Locate every uninfected red blood cell.
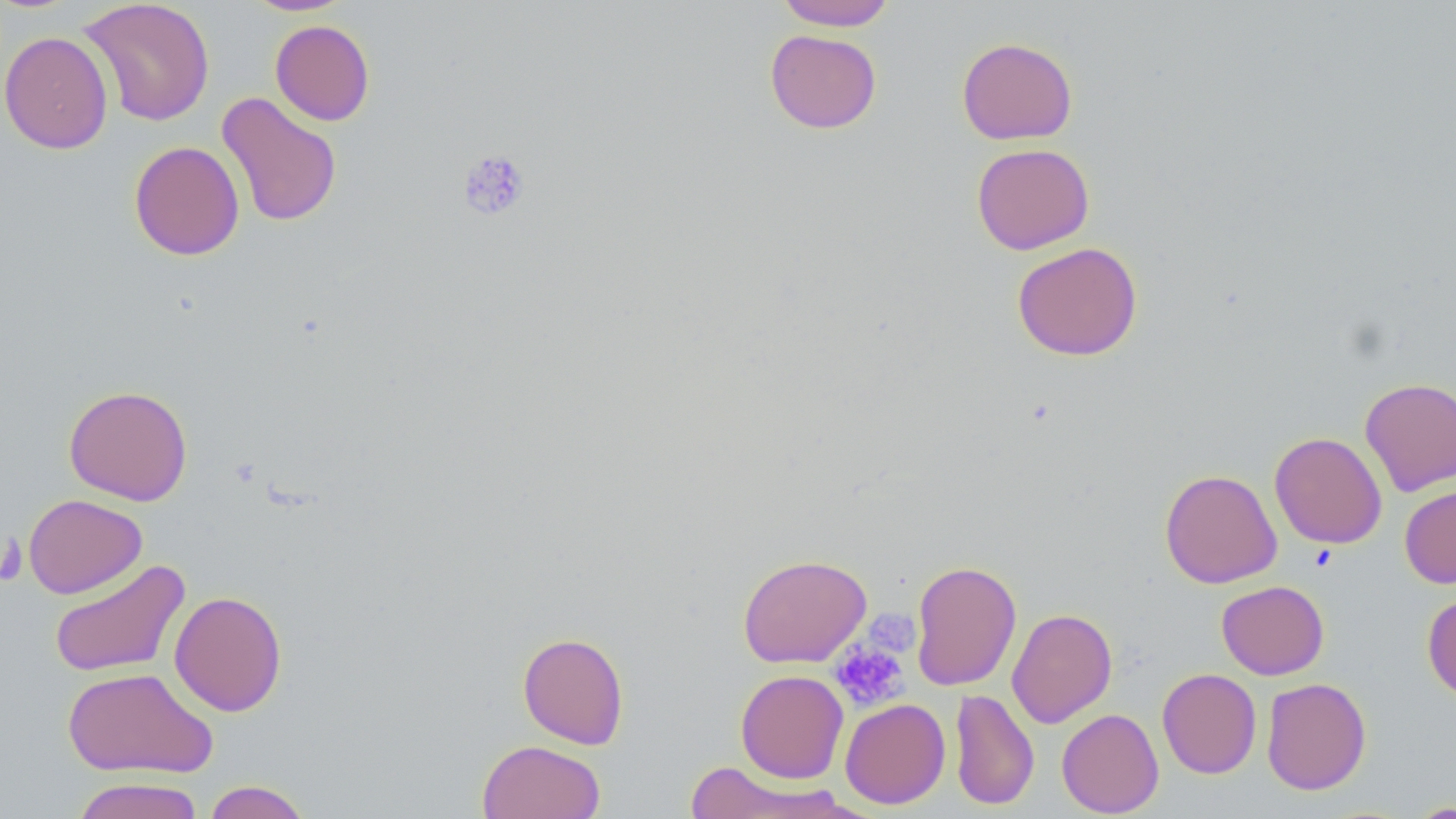
Approximate bounding boxes as [x1, y1, x2, y2] in pixels.
Uninfected red blood cells: [79, 0, 215, 127], [241, 0, 356, 16], [776, 0, 897, 31], [270, 20, 375, 126], [765, 29, 882, 133], [0, 30, 114, 154], [956, 37, 1078, 145], [216, 92, 342, 228], [129, 140, 245, 261], [971, 142, 1095, 255], [1012, 241, 1143, 361], [1360, 377, 1456, 496], [63, 385, 193, 505], [1269, 431, 1387, 549], [1159, 468, 1282, 589], [1399, 484, 1456, 589], [23, 494, 147, 599], [737, 553, 872, 668], [49, 559, 190, 679], [909, 559, 1022, 691], [1216, 580, 1329, 680], [169, 590, 287, 717], [1422, 592, 1456, 703], [1006, 608, 1118, 728], [517, 631, 630, 749], [62, 666, 217, 779], [1157, 668, 1262, 779], [735, 669, 849, 784], [1261, 677, 1372, 795], [949, 688, 1039, 810], [840, 698, 950, 809], [1056, 708, 1164, 817], [477, 740, 607, 819], [682, 762, 851, 819], [71, 776, 205, 819], [203, 780, 312, 819], [1407, 801, 1456, 818].

Platelet locations: [457, 148, 532, 222], [870, 612, 918, 659], [830, 640, 908, 711]. Slide-level diagnosis: negative for blood parasites. Light microscopy. Captured at 1000x magnification. May-Grünwald-Giemsa-stained preparation. Single field of view. Image is 1456×819 pixels. Thin blood smear.